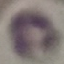
result = no malaria parasites detected
image type = automatically extracted cell patch, resized to 64 × 64 pixels
capture = smartphone through the microscope eyepiece
preparation = thin blood film
stain = Giemsa